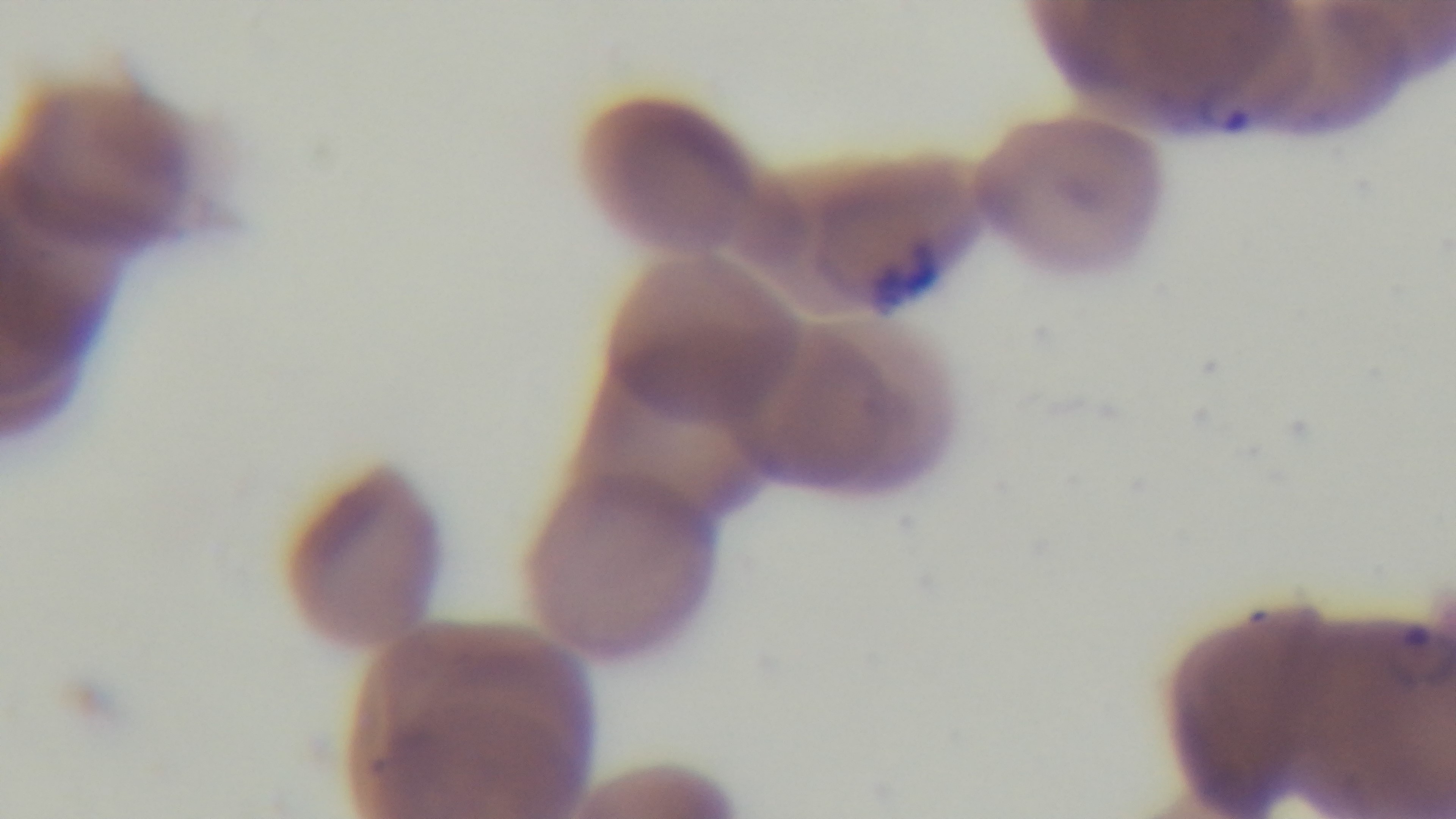
Light microscopy. Giemsa-stained. Mounted 4K digital camera. Preparation: thin blood film. One field from the slide. Oil-immersion objective, 100x. Malaria status: positive.